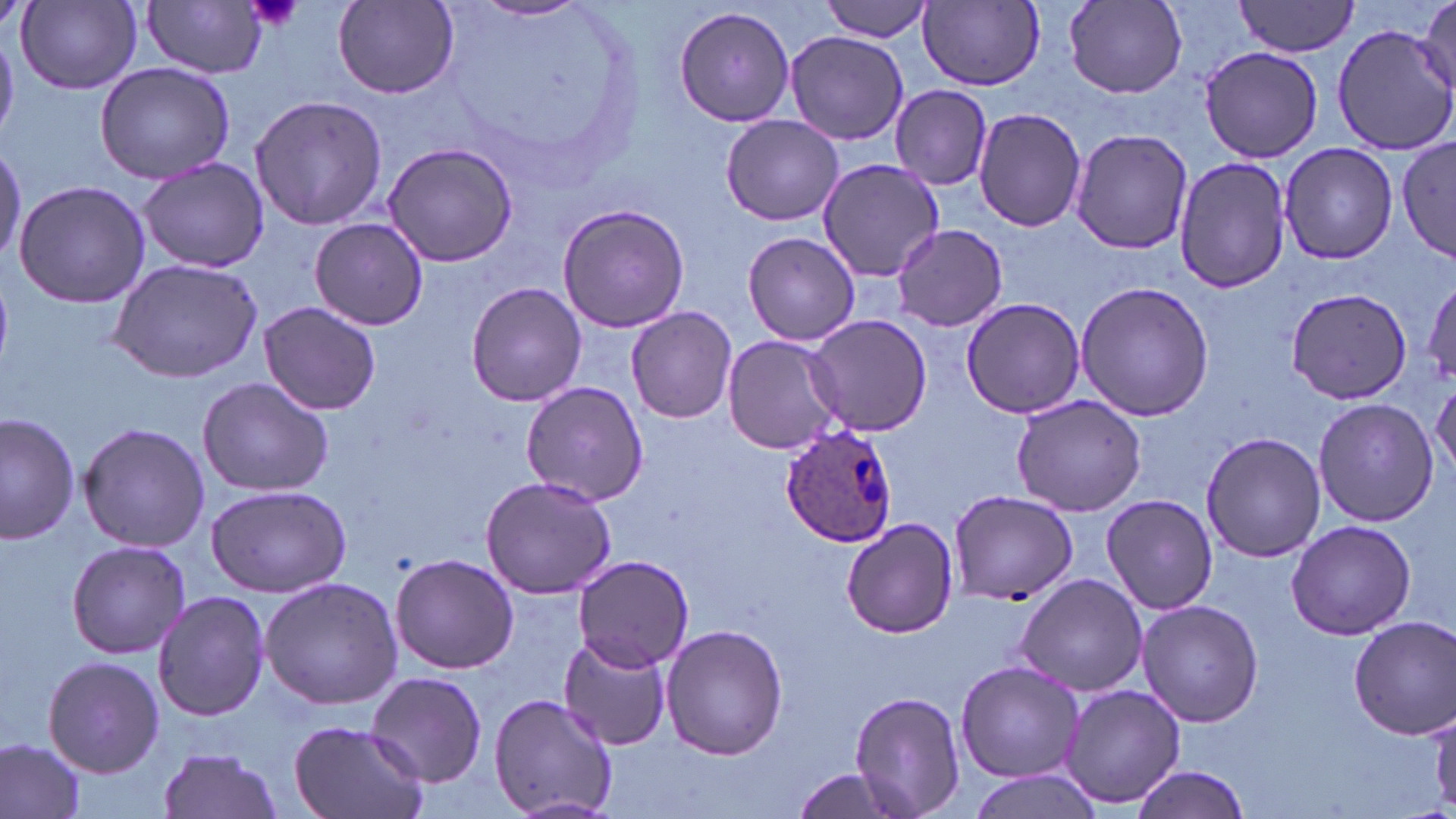

Summary:
  - Coordinate format: approximate bounding boxes as named x1/y1/x2/y2 corners in pixels
  - Plasmodium ovale-infected red blood cell locations: (x1=780, y1=423, x2=899, y2=549)
  - Uninfected red blood cell locations: (x1=819, y1=0, x2=936, y2=42), (x1=916, y1=0, x2=1046, y2=93), (x1=1061, y1=0, x2=1190, y2=100), (x1=1235, y1=0, x2=1358, y2=57), (x1=16, y1=1, x2=143, y2=92), (x1=145, y1=1, x2=269, y2=77), (x1=332, y1=1, x2=461, y2=100), (x1=474, y1=1, x2=590, y2=23), (x1=1414, y1=4, x2=1456, y2=104), (x1=674, y1=5, x2=798, y2=129), (x1=1331, y1=24, x2=1456, y2=155), (x1=785, y1=31, x2=910, y2=146), (x1=1198, y1=44, x2=1322, y2=163), (x1=95, y1=61, x2=235, y2=185), (x1=890, y1=85, x2=992, y2=189), (x1=249, y1=94, x2=386, y2=231), (x1=973, y1=107, x2=1087, y2=231), (x1=720, y1=114, x2=844, y2=227), (x1=1070, y1=130, x2=1193, y2=256), (x1=0, y1=138, x2=25, y2=268), (x1=1396, y1=138, x2=1453, y2=263), (x1=1279, y1=141, x2=1396, y2=265), (x1=383, y1=143, x2=520, y2=267), (x1=1173, y1=156, x2=1291, y2=295), (x1=137, y1=157, x2=269, y2=273), (x1=815, y1=157, x2=945, y2=282), (x1=13, y1=180, x2=151, y2=308), (x1=557, y1=203, x2=691, y2=334), (x1=309, y1=218, x2=430, y2=330), (x1=892, y1=223, x2=1008, y2=332), (x1=743, y1=231, x2=859, y2=347), (x1=108, y1=258, x2=264, y2=383), (x1=1420, y1=273, x2=1456, y2=391), (x1=1075, y1=279, x2=1214, y2=422), (x1=464, y1=281, x2=588, y2=407), (x1=1287, y1=286, x2=1410, y2=405), (x1=960, y1=297, x2=1087, y2=419), (x1=260, y1=301, x2=380, y2=417), (x1=625, y1=306, x2=738, y2=423), (x1=805, y1=313, x2=933, y2=437), (x1=721, y1=335, x2=847, y2=455), (x1=196, y1=377, x2=334, y2=497), (x1=1430, y1=379, x2=1456, y2=479), (x1=519, y1=380, x2=649, y2=505), (x1=1010, y1=395, x2=1146, y2=518), (x1=1312, y1=396, x2=1438, y2=529), (x1=0, y1=412, x2=79, y2=545), (x1=78, y1=422, x2=210, y2=552), (x1=1202, y1=430, x2=1324, y2=563), (x1=480, y1=475, x2=618, y2=599), (x1=206, y1=483, x2=354, y2=598), (x1=949, y1=489, x2=1075, y2=604), (x1=1100, y1=494, x2=1218, y2=615), (x1=841, y1=518, x2=959, y2=639), (x1=1286, y1=519, x2=1417, y2=641), (x1=66, y1=539, x2=193, y2=659), (x1=390, y1=553, x2=518, y2=675), (x1=573, y1=554, x2=696, y2=673), (x1=1013, y1=572, x2=1151, y2=697), (x1=260, y1=577, x2=404, y2=709), (x1=152, y1=591, x2=270, y2=721), (x1=1134, y1=601, x2=1265, y2=727), (x1=1349, y1=617, x2=1455, y2=740), (x1=660, y1=623, x2=786, y2=758), (x1=556, y1=635, x2=670, y2=750), (x1=42, y1=655, x2=163, y2=776), (x1=956, y1=660, x2=1083, y2=783), (x1=366, y1=670, x2=488, y2=787), (x1=1059, y1=683, x2=1186, y2=810), (x1=849, y1=691, x2=966, y2=818), (x1=488, y1=693, x2=619, y2=819), (x1=287, y1=721, x2=428, y2=819), (x1=0, y1=736, x2=86, y2=819), (x1=155, y1=747, x2=286, y2=819), (x1=1126, y1=763, x2=1250, y2=818), (x1=786, y1=769, x2=916, y2=817), (x1=962, y1=770, x2=1102, y2=819)
  - Platelet locations: (x1=243, y1=0, x2=304, y2=32)
  - Slide-level diagnosis: Plasmodium ovale
  - Stain: May-Grünwald-Giemsa
  - Field of view: one of a larger specimen
  - Image size: 1456×819 pixels
  - Magnification: 1000x
  - Preparation: thin blood film
  - Modality: optical microscopy